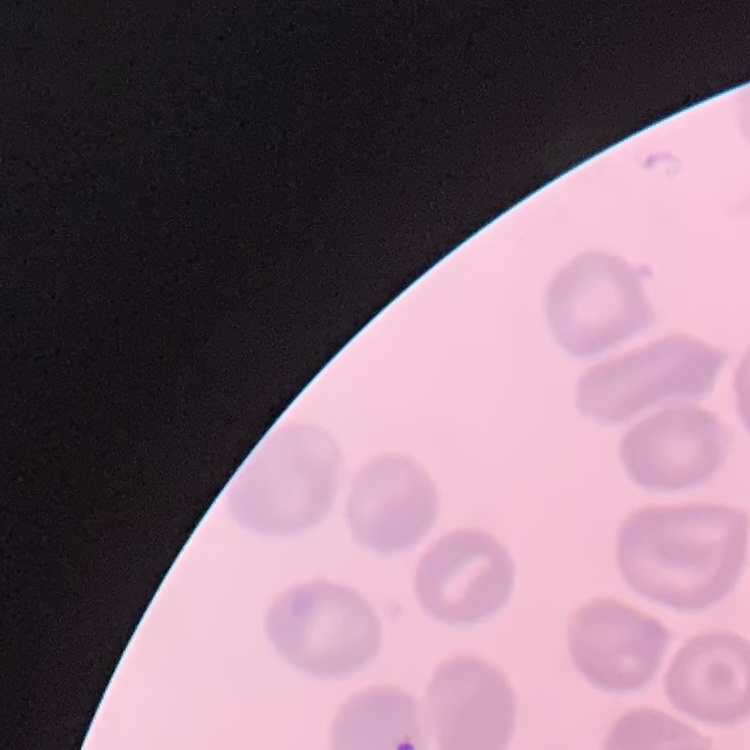
{
  "red_blood_cell_morphology": "no rouleaux formation",
  "preparation": "thin peripheral smear",
  "image_type": "square crop of a larger photomicrograph",
  "stain": "Field's or Giemsa"
}